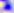

Summary:
  - Magnification: 400x
  - Identification: Toxoplasma gondii
  - Modality: photomicrograph